Locate platelets.
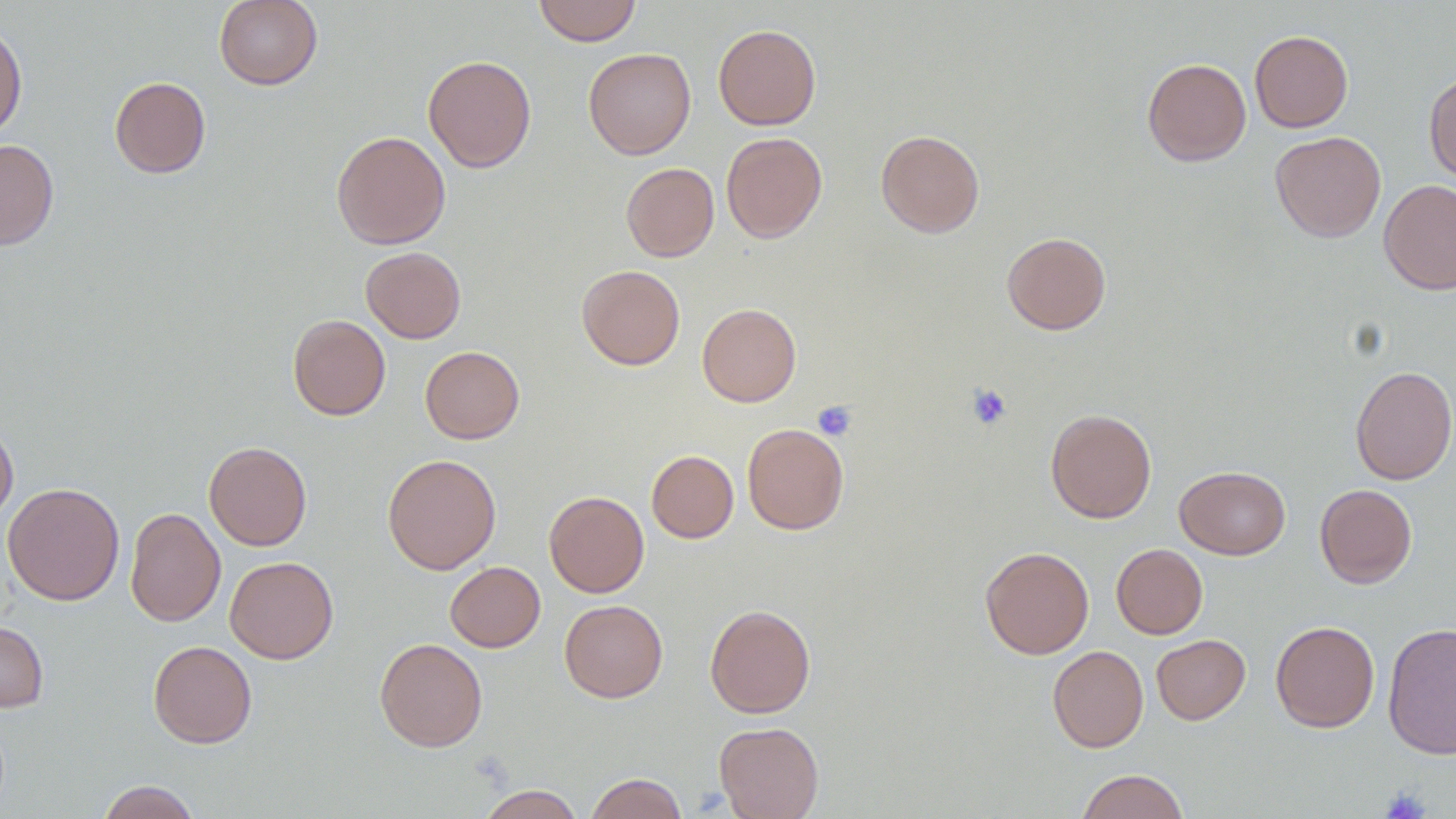

Approximate bounding boxes as (x1, y1, x2, y2) in pixels.
Platelets: (967, 383, 1012, 430), (814, 400, 857, 441), (1380, 787, 1430, 818).

slide-level diagnosis = no evidence of blood parasites
magnification = 1000x
field of view = one of a larger specimen
uninfected red blood cell locations = approximate bounding boxes as (x1, y1, x2, y2) in pixels: (214, 0, 323, 90), (533, 0, 641, 46), (0, 22, 27, 140), (713, 24, 821, 130), (1249, 30, 1353, 133), (583, 47, 696, 160), (423, 54, 537, 172), (1142, 58, 1251, 166), (1424, 72, 1456, 182), (109, 76, 211, 178), (875, 129, 985, 238), (331, 130, 451, 249), (1270, 131, 1386, 243), (721, 132, 828, 243), (0, 138, 59, 251), (621, 163, 719, 262), (1378, 178, 1456, 295), (1002, 231, 1111, 334), (361, 246, 466, 343), (576, 264, 685, 370), (697, 303, 801, 407), (288, 314, 391, 420), (420, 346, 525, 444), (1350, 365, 1456, 485), (1045, 408, 1156, 523), (0, 417, 18, 525), (742, 423, 849, 535), (204, 441, 312, 551), (646, 450, 738, 543), (382, 453, 502, 574), (1174, 466, 1290, 559), (2, 482, 124, 606), (1314, 484, 1417, 588), (544, 491, 649, 597), (124, 507, 226, 627), (1111, 543, 1208, 639), (979, 546, 1094, 659), (225, 556, 338, 663), (445, 561, 545, 652), (559, 599, 668, 703), (705, 604, 815, 718), (0, 619, 49, 712), (1270, 620, 1380, 733), (1382, 622, 1456, 760), (1151, 634, 1250, 725), (374, 637, 487, 752), (148, 640, 257, 748), (1047, 645, 1148, 752), (714, 721, 824, 818), (1076, 769, 1190, 819), (585, 772, 687, 819), (97, 780, 201, 819), (475, 784, 585, 818)
modality = light microscopy
preparation = thin blood smear
image size = 1456×819 pixels